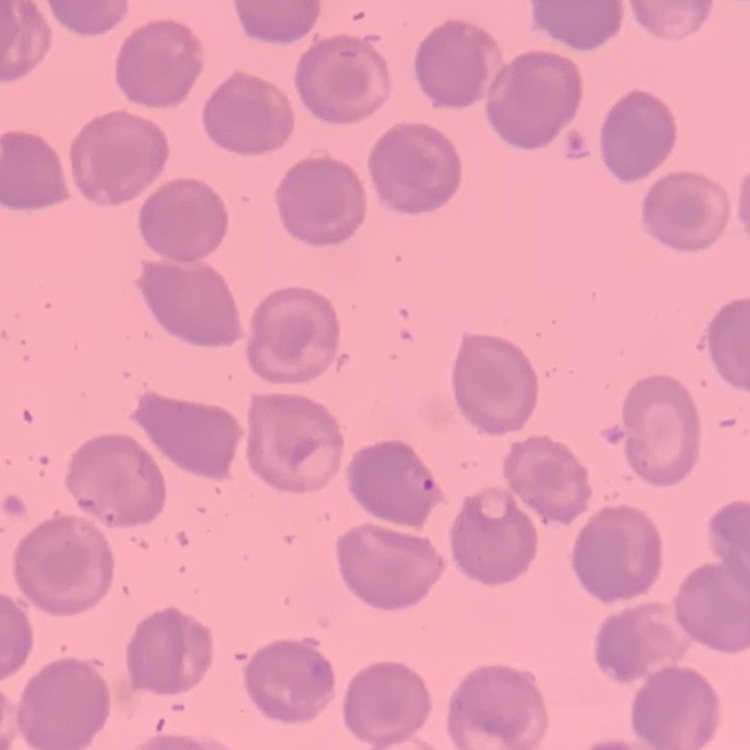

Summary:
  - Red blood cell morphology: no rouleaux formation
  - Image type: one tile cut from a larger photomicrograph
  - Preparation: thin peripheral smear
  - Stain: Field's or Giemsa